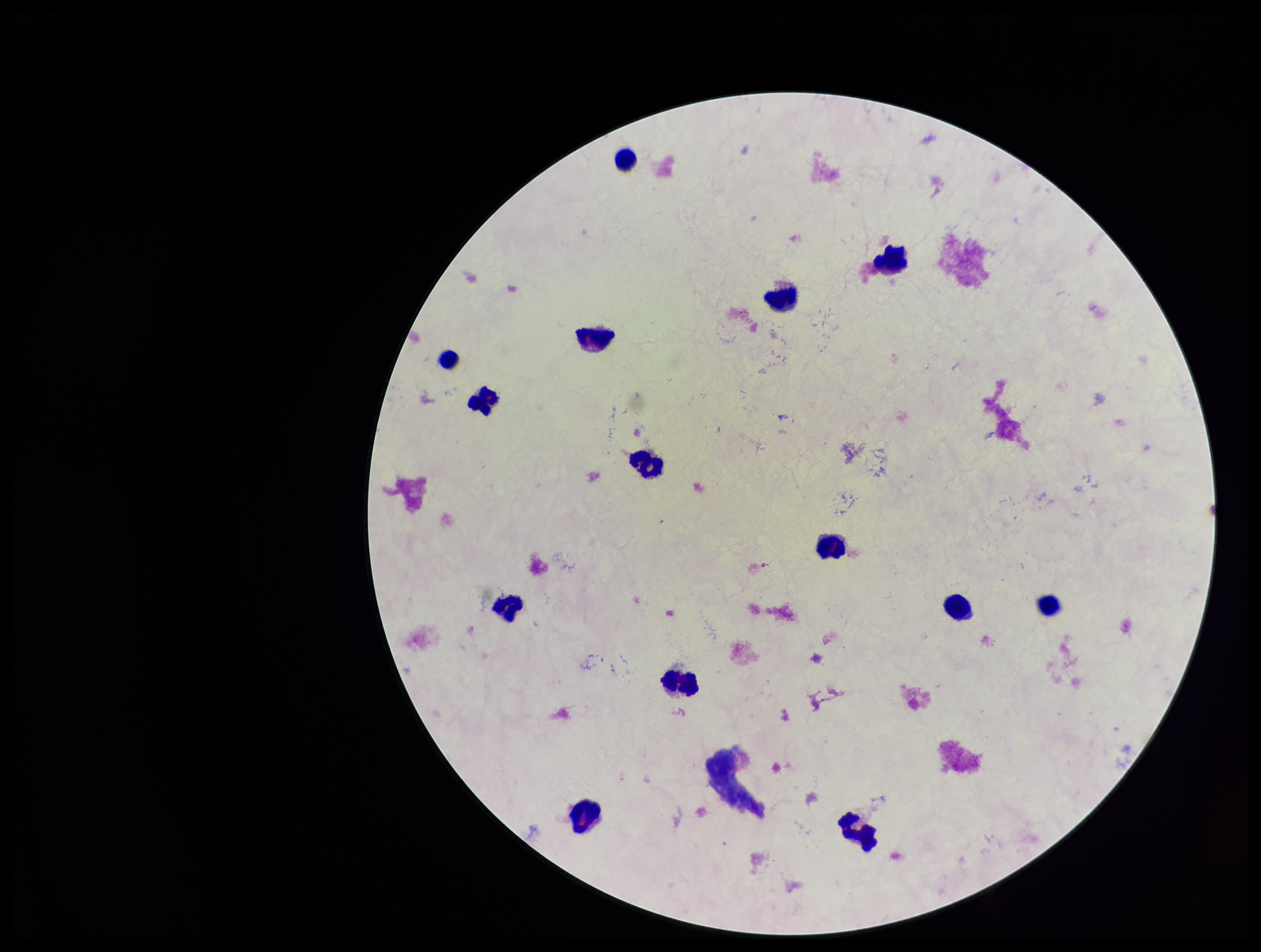

stain: Giemsa
patient_malaria_status: negative
plasmodium_parasites: none identified
image_size: 1261×952 pixels
leukocyte_count: 14
parasite_count: 0
preparation: thick blood smear
field_of_view: single
capture: smartphone photograph through the microscope eyepiece